Name the cell type shown.
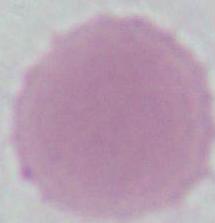

This is an erythrocyte.

Photomicrograph. 1000x magnification.